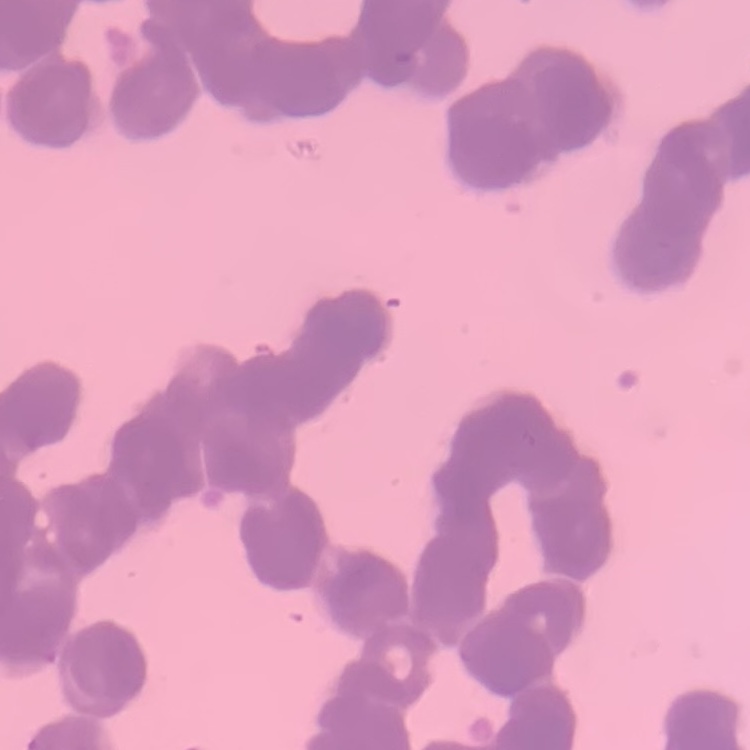
Summary:
  - Red blood cell morphology: rouleaux formation
  - Preparation: thin peripheral smear
  - Image type: square crop of a larger photomicrograph
  - Stain: Field's or Giemsa